Classify this cell by malaria status.
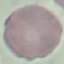

Uninfected.

Summary:
  - Stain: Giemsa
  - Capture: smartphone camera at the microscope eyepiece
  - Preparation: thin smear
  - Image type: cell patch, automatically extracted from a larger field of view and resized to 64 × 64 pixels